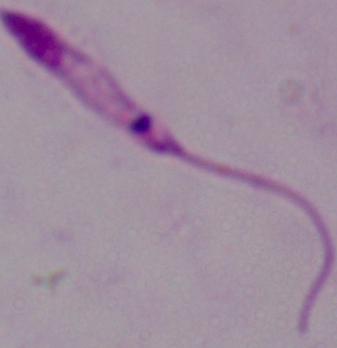

modality = micrograph
magnification = 1000x
identification = Leishmania